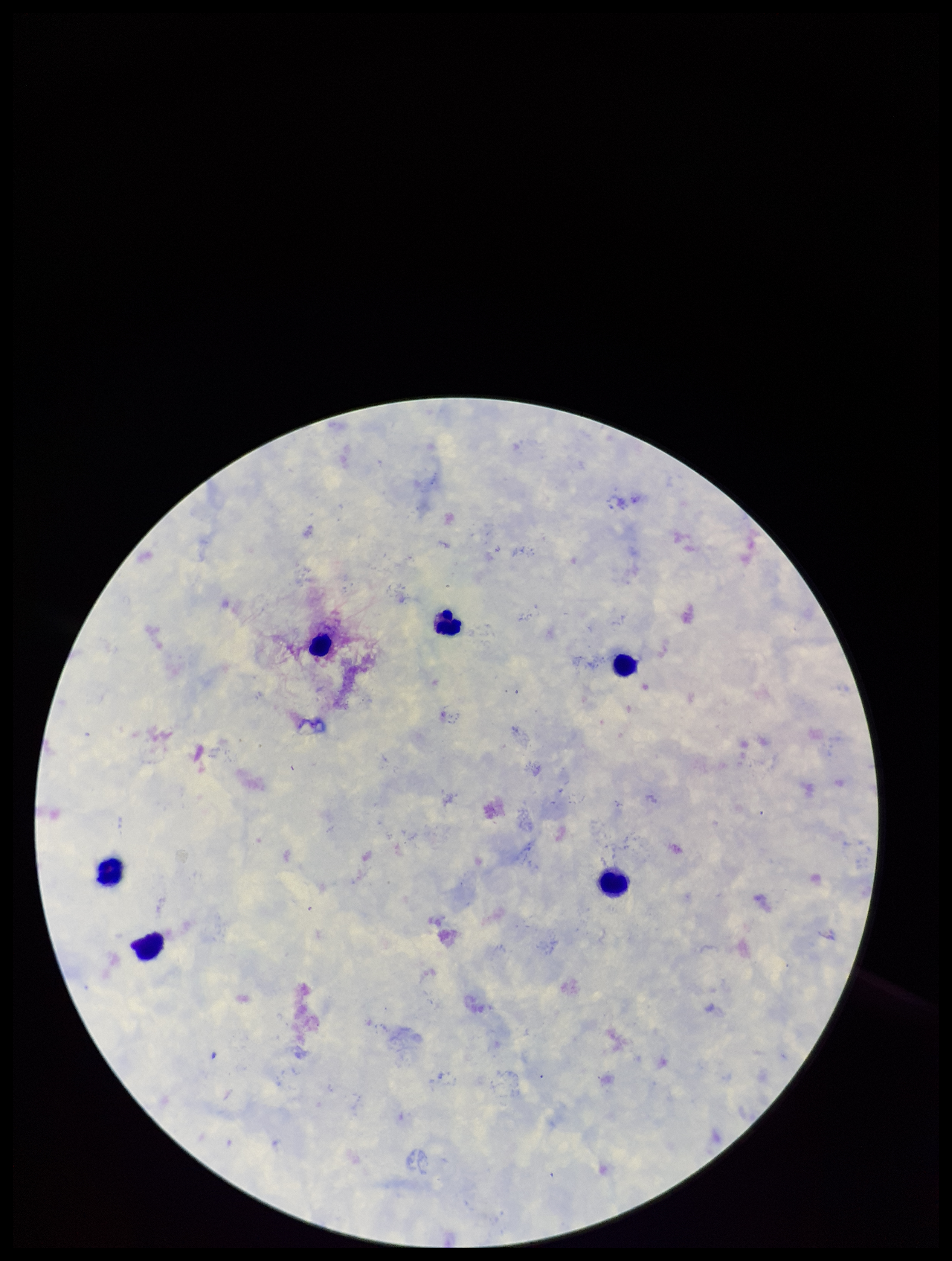 Stained with Giemsa. Single field of view. Image is 952×1261 pixels. Leukocyte count: 6. Preparation: thick. Parasite count: 0. Patient malaria status: negative. Plasmodium parasites: none seen. Smartphone photograph taken through the eyepiece of a microscope.